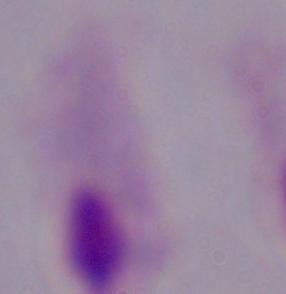
Captured at 1000x magnification. A trichomonad is shown. Micrograph.